Outline each uninfected red blood cell.
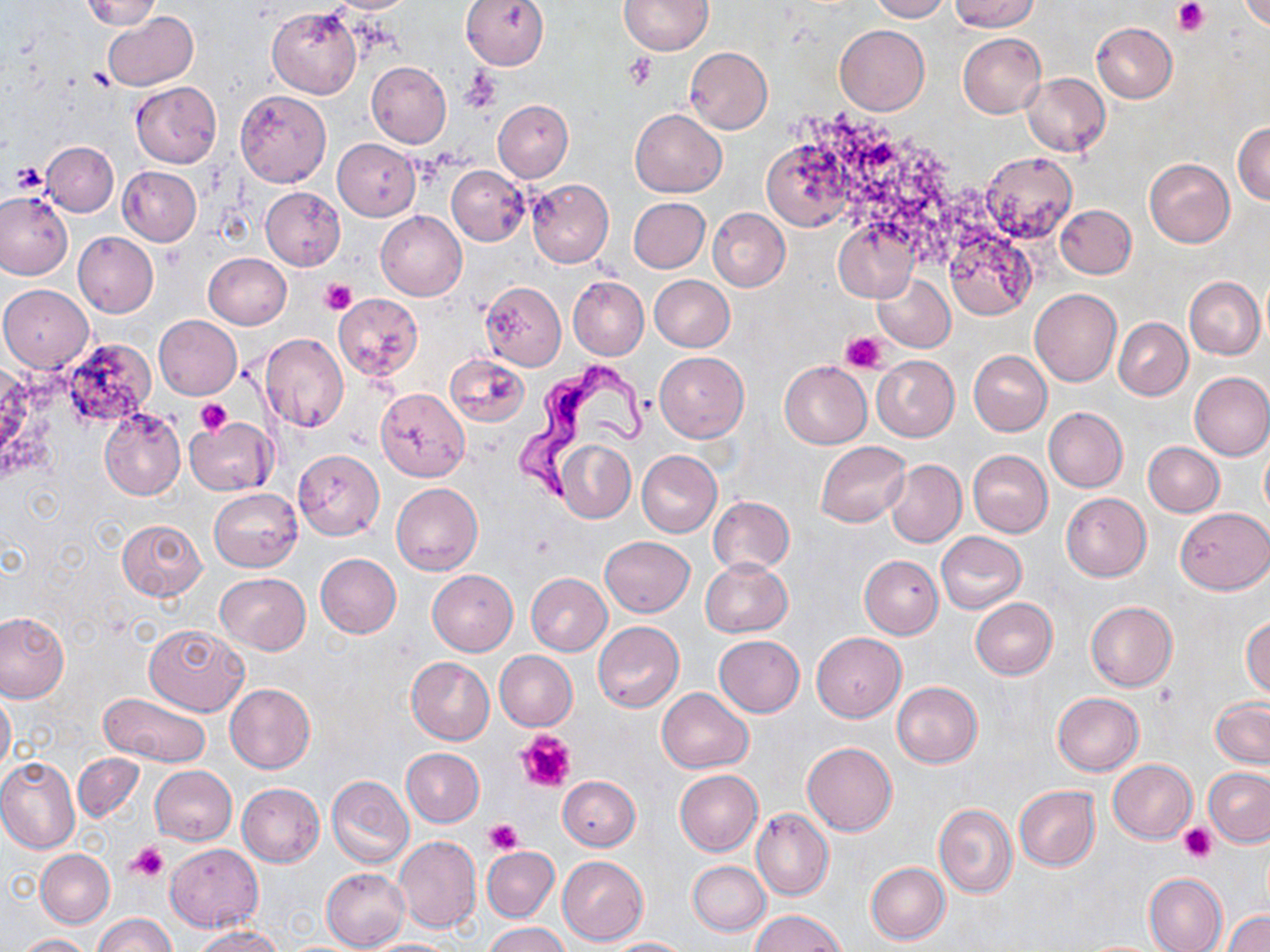

Approximate bounding boxes as named x1/y1/x2/y2 corners in pixels.
Uninfected red blood cells: (x1=80, y1=0, x2=162, y2=29), (x1=323, y1=0, x2=420, y2=13), (x1=460, y1=0, x2=549, y2=70), (x1=618, y1=0, x2=713, y2=55), (x1=868, y1=0, x2=951, y2=22), (x1=950, y1=0, x2=1039, y2=32), (x1=1238, y1=0, x2=1269, y2=31), (x1=267, y1=6, x2=361, y2=98), (x1=101, y1=10, x2=198, y2=90), (x1=1091, y1=22, x2=1177, y2=102), (x1=835, y1=25, x2=930, y2=115), (x1=958, y1=33, x2=1047, y2=119), (x1=684, y1=47, x2=773, y2=134), (x1=366, y1=61, x2=452, y2=148), (x1=1022, y1=72, x2=1110, y2=156), (x1=130, y1=82, x2=222, y2=168), (x1=235, y1=89, x2=331, y2=186), (x1=494, y1=100, x2=573, y2=181), (x1=630, y1=109, x2=727, y2=197), (x1=1233, y1=120, x2=1270, y2=206), (x1=762, y1=137, x2=857, y2=232), (x1=332, y1=139, x2=421, y2=220), (x1=42, y1=141, x2=118, y2=216), (x1=980, y1=151, x2=1077, y2=243), (x1=1144, y1=158, x2=1235, y2=247), (x1=118, y1=166, x2=202, y2=245), (x1=447, y1=166, x2=529, y2=245), (x1=526, y1=179, x2=614, y2=267), (x1=260, y1=186, x2=345, y2=269), (x1=0, y1=192, x2=73, y2=279), (x1=629, y1=197, x2=710, y2=273), (x1=634, y1=198, x2=716, y2=352), (x1=1055, y1=205, x2=1136, y2=279), (x1=707, y1=208, x2=790, y2=292), (x1=376, y1=210, x2=467, y2=301), (x1=833, y1=219, x2=920, y2=303), (x1=850, y1=228, x2=941, y2=337), (x1=944, y1=229, x2=1035, y2=320), (x1=73, y1=232, x2=159, y2=316), (x1=203, y1=252, x2=291, y2=330), (x1=873, y1=271, x2=955, y2=353), (x1=649, y1=275, x2=735, y2=352), (x1=567, y1=276, x2=648, y2=360), (x1=1185, y1=276, x2=1265, y2=358), (x1=479, y1=281, x2=566, y2=370), (x1=1, y1=284, x2=93, y2=371), (x1=1030, y1=289, x2=1122, y2=387), (x1=333, y1=294, x2=423, y2=380), (x1=153, y1=315, x2=242, y2=399), (x1=1114, y1=316, x2=1192, y2=400), (x1=261, y1=333, x2=349, y2=432), (x1=968, y1=351, x2=1052, y2=437), (x1=655, y1=352, x2=748, y2=441), (x1=446, y1=354, x2=529, y2=427), (x1=872, y1=356, x2=959, y2=442), (x1=779, y1=361, x2=872, y2=449), (x1=1189, y1=371, x2=1270, y2=461), (x1=376, y1=388, x2=469, y2=480), (x1=1042, y1=406, x2=1127, y2=493), (x1=99, y1=408, x2=185, y2=499), (x1=184, y1=417, x2=275, y2=496), (x1=816, y1=439, x2=910, y2=527), (x1=555, y1=440, x2=636, y2=522), (x1=1143, y1=442, x2=1224, y2=517), (x1=1260, y1=442, x2=1270, y2=519), (x1=293, y1=449, x2=383, y2=540), (x1=968, y1=450, x2=1053, y2=538), (x1=637, y1=451, x2=721, y2=537), (x1=884, y1=458, x2=966, y2=548), (x1=391, y1=482, x2=483, y2=575), (x1=209, y1=488, x2=302, y2=571), (x1=1060, y1=492, x2=1151, y2=582), (x1=707, y1=497, x2=794, y2=574), (x1=1176, y1=508, x2=1270, y2=595), (x1=117, y1=519, x2=206, y2=600), (x1=935, y1=531, x2=1027, y2=615), (x1=600, y1=536, x2=694, y2=616), (x1=315, y1=553, x2=401, y2=638), (x1=860, y1=555, x2=942, y2=639), (x1=700, y1=558, x2=794, y2=638), (x1=428, y1=570, x2=517, y2=655), (x1=215, y1=572, x2=309, y2=653), (x1=525, y1=574, x2=612, y2=656), (x1=971, y1=598, x2=1057, y2=679), (x1=1085, y1=601, x2=1177, y2=692), (x1=0, y1=613, x2=69, y2=702), (x1=1242, y1=616, x2=1270, y2=699), (x1=594, y1=621, x2=684, y2=711), (x1=143, y1=623, x2=248, y2=715), (x1=812, y1=632, x2=905, y2=722), (x1=713, y1=636, x2=804, y2=718), (x1=494, y1=651, x2=578, y2=731), (x1=406, y1=657, x2=494, y2=745), (x1=892, y1=681, x2=983, y2=768), (x1=225, y1=684, x2=315, y2=773), (x1=657, y1=687, x2=753, y2=772), (x1=0, y1=688, x2=14, y2=775), (x1=98, y1=692, x2=209, y2=769), (x1=1052, y1=692, x2=1144, y2=774), (x1=1211, y1=699, x2=1269, y2=767), (x1=802, y1=742, x2=897, y2=837), (x1=401, y1=748, x2=484, y2=827), (x1=74, y1=754, x2=144, y2=822), (x1=0, y1=757, x2=81, y2=854), (x1=1108, y1=759, x2=1196, y2=843), (x1=150, y1=766, x2=237, y2=845), (x1=1204, y1=767, x2=1270, y2=846), (x1=674, y1=770, x2=761, y2=856), (x1=326, y1=776, x2=414, y2=868), (x1=558, y1=776, x2=640, y2=851), (x1=236, y1=783, x2=325, y2=866), (x1=1013, y1=786, x2=1100, y2=870), (x1=934, y1=804, x2=1018, y2=898), (x1=752, y1=809, x2=834, y2=901), (x1=393, y1=836, x2=481, y2=933), (x1=164, y1=843, x2=262, y2=931), (x1=481, y1=846, x2=559, y2=922), (x1=36, y1=849, x2=114, y2=927), (x1=557, y1=855, x2=649, y2=945), (x1=688, y1=861, x2=770, y2=936), (x1=866, y1=862, x2=949, y2=944), (x1=321, y1=868, x2=410, y2=950), (x1=1143, y1=873, x2=1227, y2=952), (x1=751, y1=911, x2=847, y2=952), (x1=1223, y1=911, x2=1270, y2=952), (x1=93, y1=913, x2=177, y2=952), (x1=484, y1=923, x2=569, y2=952), (x1=190, y1=926, x2=282, y2=951), (x1=15, y1=933, x2=93, y2=952), (x1=604, y1=937, x2=691, y2=951), (x1=361, y1=938, x2=461, y2=952).

{
  "slide_level_diagnosis": "Trypanosoma brucei",
  "image_size": "1270×952 pixels",
  "stain": "May-Grünwald-Giemsa",
  "magnification": "1000x",
  "trypanosoma_brucei_locations": "approximate bounding boxes as named x1/y1/x2/y2 corners in pixels: (x1=512, y1=361, x2=651, y2=507)",
  "platelet_locations": "approximate bounding boxes as named x1/y1/x2/y2 corners in pixels: (x1=1172, y1=0, x2=1210, y2=37), (x1=624, y1=54, x2=658, y2=90), (x1=461, y1=68, x2=501, y2=112), (x1=8, y1=160, x2=50, y2=195), (x1=321, y1=278, x2=355, y2=315), (x1=840, y1=333, x2=888, y2=374), (x1=195, y1=398, x2=233, y2=435), (x1=515, y1=729, x2=576, y2=792), (x1=483, y1=818, x2=524, y2=856), (x1=1178, y1=823, x2=1216, y2=862), (x1=125, y1=842, x2=168, y2=882)",
  "preparation": "thin blood smear",
  "field_of_view": "one of a larger specimen",
  "modality": "optical microscopy"
}